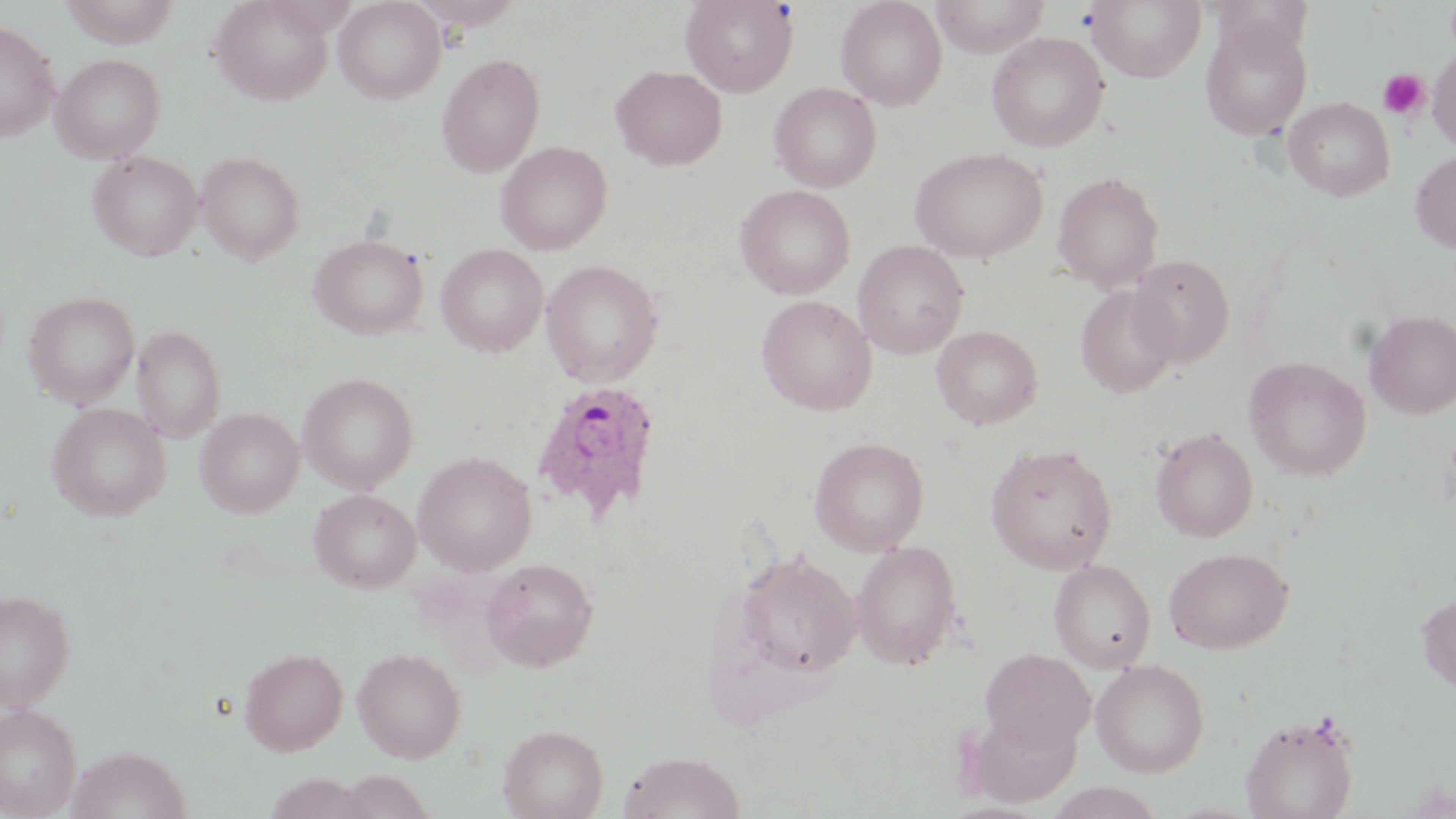 Approximate bounding boxes as [x1, y1, x2, y2] in pixels. Uninfected red blood cell locations: [210, 0, 335, 105], [333, 0, 445, 103], [680, 0, 798, 96], [835, 0, 946, 110], [930, 0, 1049, 57], [1086, 0, 1207, 82], [58, 1, 180, 47], [1200, 17, 1312, 140], [0, 21, 59, 140], [986, 32, 1109, 152], [1428, 46, 1456, 152], [436, 52, 545, 178], [50, 53, 166, 163], [610, 64, 727, 170], [769, 83, 881, 192], [1283, 97, 1395, 201], [495, 140, 612, 254], [910, 146, 1048, 263], [88, 150, 202, 260], [1410, 150, 1456, 253], [196, 151, 305, 263], [1051, 170, 1164, 293], [735, 185, 855, 299], [309, 233, 429, 339], [853, 240, 969, 360], [435, 244, 548, 357], [1127, 254, 1235, 368], [540, 259, 664, 387], [1075, 286, 1178, 398], [23, 290, 139, 408], [756, 295, 876, 415], [1364, 310, 1456, 418], [131, 325, 225, 442], [931, 325, 1043, 429], [1244, 356, 1371, 481], [297, 372, 419, 494], [46, 402, 171, 521], [195, 408, 304, 516], [1150, 427, 1258, 543], [808, 436, 929, 556], [985, 442, 1118, 575], [412, 450, 537, 575], [309, 489, 421, 592], [850, 540, 963, 671], [1164, 547, 1292, 653], [733, 550, 860, 679], [480, 557, 599, 672], [1049, 560, 1156, 672], [0, 588, 75, 710], [1416, 593, 1456, 695], [238, 646, 348, 756], [352, 647, 465, 762], [979, 648, 1096, 752], [1090, 659, 1209, 777], [0, 703, 81, 817], [967, 708, 1082, 806], [1240, 711, 1359, 819], [498, 724, 608, 819], [67, 745, 191, 819], [617, 750, 747, 819], [333, 771, 434, 819], [1045, 782, 1164, 819]. Plasmodium ovale-infected red blood cell locations: [530, 379, 663, 523]. Platelet locations: [1378, 69, 1430, 119]. Slide-level diagnosis: Plasmodium ovale. 1000x magnification. Single field of view. Thin blood film. Light microscopy. Image is 1456×819 pixels. May-Grünwald-Giemsa-stained preparation.